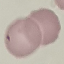
Summary:
  - Malaria status: uninfected
  - Capture: smartphone through the microscope eyepiece
  - Preparation: thin blood smear
  - Stain: Giemsa
  - Image type: automatically extracted cell patch, resized to 64 × 64 pixels